Name the parasite shown.
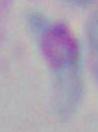

This is Toxoplasma gondii.

modality = photomicrograph
magnification = 1000x